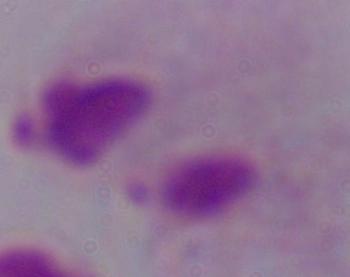
modality = photomicrograph
magnification = 1000x
identification = trichomonad